State which cell type is depicted.
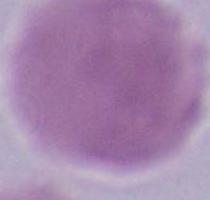
An erythrocyte.

magnification: 1000x
modality: photomicrograph